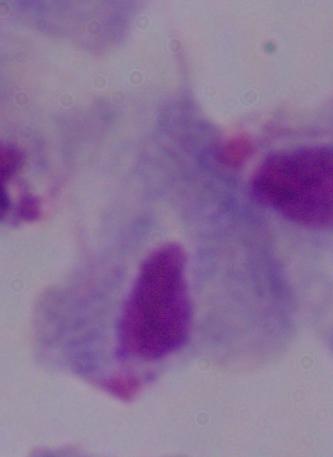 Captured at 1000x magnification. A trichomonad is seen. Micrograph.